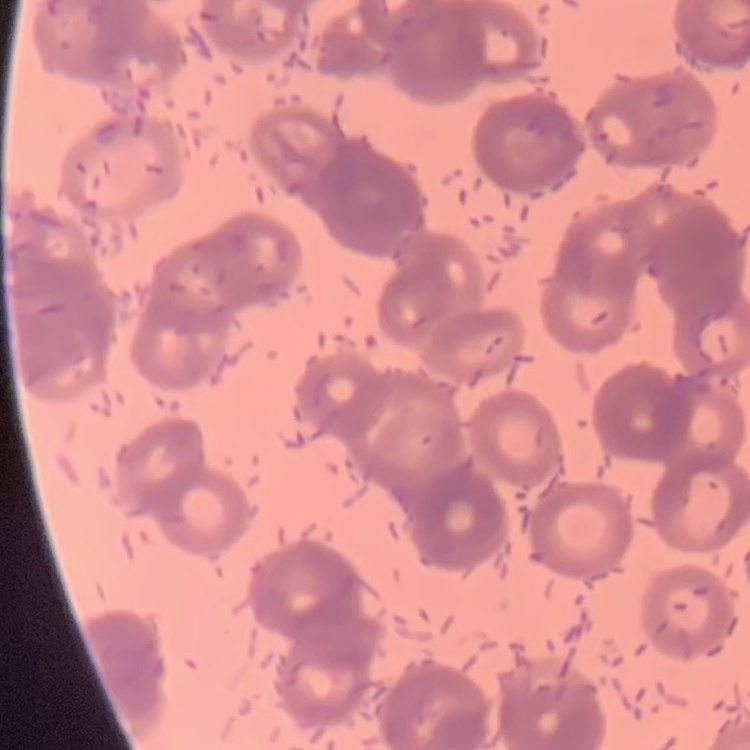
Summary:
  - Red blood cell morphology: rouleaux formation
  - Image type: square crop of a larger photomicrograph
  - Preparation: thin blood smear
  - Stain: Field's or Giemsa